Point out each malaria parasite.
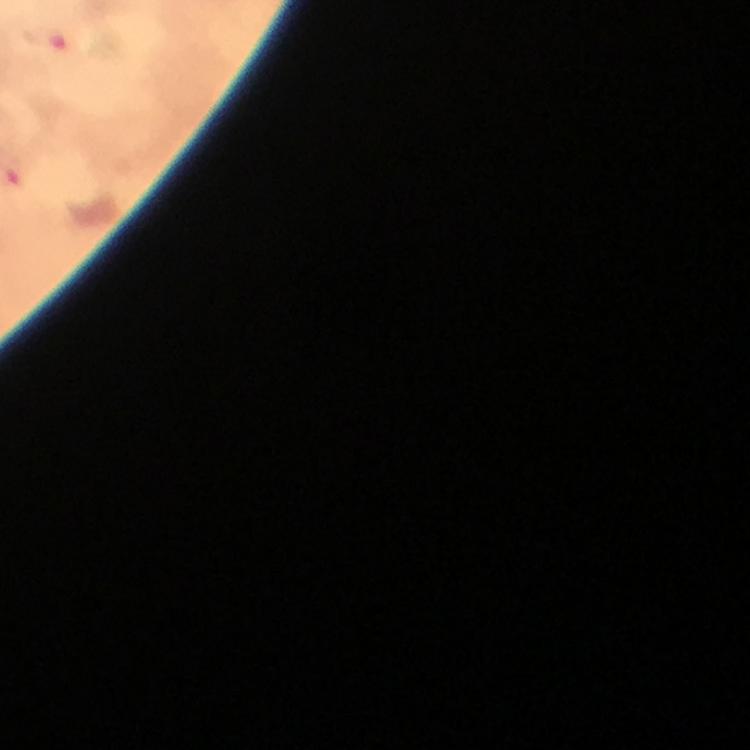
Approximate centers as {x, y} in pixels.
Malaria parasites: {46, 38}.

100x magnification. Immersion oil was used. Giemsa stain. Photographed with a smartphone mounted on the microscope. From a malaria diagnostic workup. Thick blood film. A crop from one field of view. Image is 750×750 pixels.